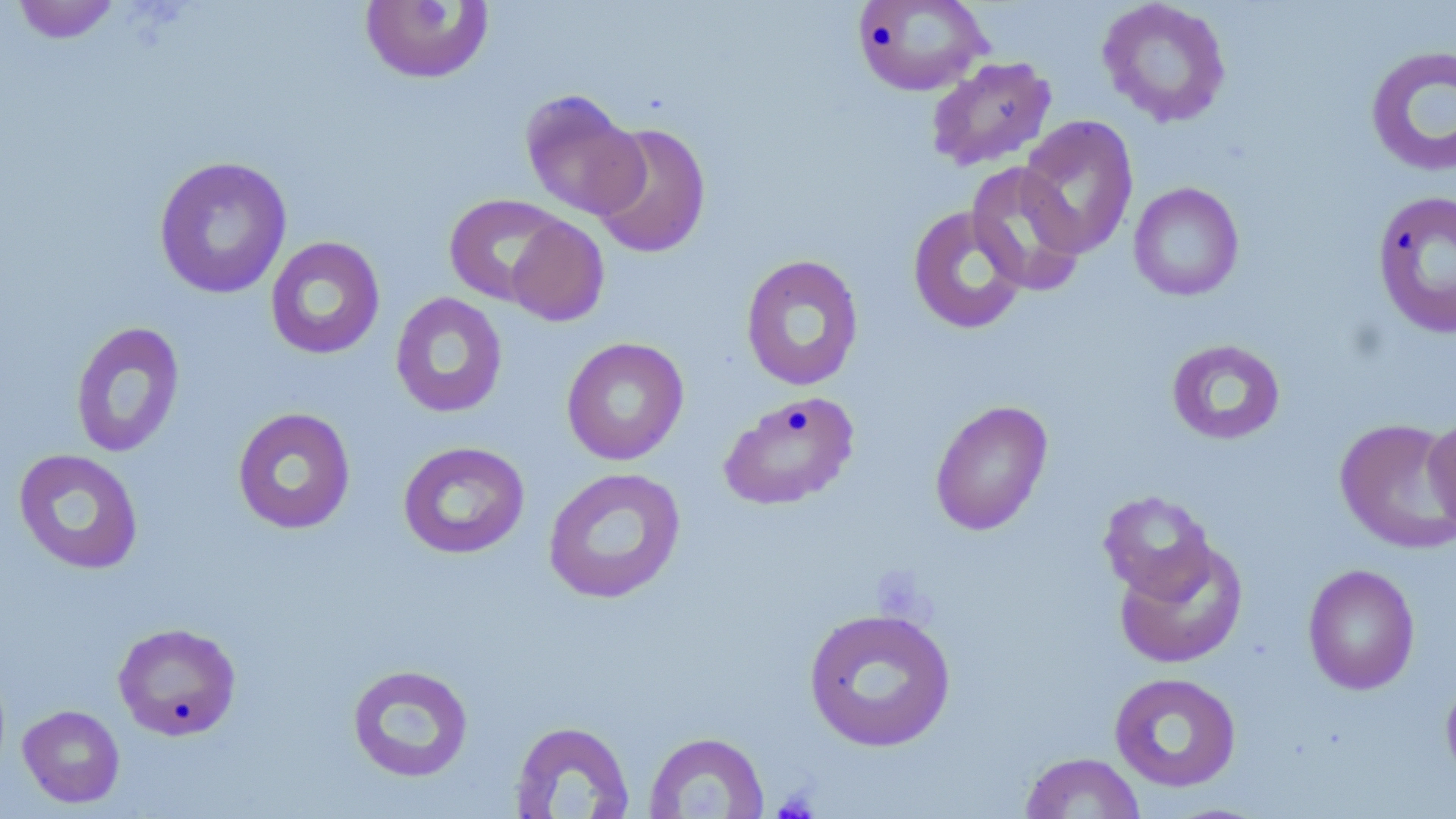

Approximate bounding boxes as (x1, y1, x2, y2) in pixels. Uninfected red blood cell locations: (10, 0, 123, 44), (852, 0, 991, 96), (1097, 0, 1232, 128), (359, 1, 495, 85), (1364, 44, 1456, 177), (926, 56, 1057, 172), (519, 89, 648, 220), (1017, 115, 1139, 259), (590, 122, 712, 259), (154, 156, 293, 300), (965, 161, 1088, 297), (1129, 181, 1244, 301), (1371, 188, 1456, 339), (443, 193, 569, 306), (907, 205, 1029, 335), (506, 216, 610, 327), (264, 236, 385, 360), (740, 255, 864, 392), (389, 292, 508, 418), (69, 321, 185, 458), (561, 337, 690, 466), (1165, 338, 1286, 446), (718, 390, 860, 511), (930, 399, 1053, 536), (232, 407, 357, 535), (1423, 412, 1456, 541), (1334, 418, 1456, 554), (397, 441, 530, 560), (13, 449, 144, 575), (542, 467, 687, 604), (1098, 490, 1217, 601), (1114, 539, 1249, 669), (1302, 563, 1421, 695), (803, 606, 956, 752), (113, 622, 243, 740), (346, 663, 474, 784), (1108, 671, 1242, 792), (1440, 672, 1456, 789), (18, 704, 126, 808), (508, 720, 635, 818), (643, 731, 769, 818), (1020, 752, 1146, 818). Platelet locations: (879, 576, 928, 624), (775, 789, 819, 819). Slide-level diagnosis: negative for blood parasites. May-Grünwald-Giemsa-stained preparation. Thin blood film. Captured at 1000x magnification. Light microscopy. Single field of view. Image is 1456×819 pixels.